Classify this cell by malaria status.
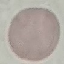
Uninfected.

capture = smartphone camera at the microscope eyepiece
image type = automatically extracted cell patch, resized to 64 × 64 pixels
preparation = thin blood smear
stain = Giemsa